Report the malaria status of this cell.
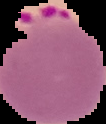
It is parasitized.

Summary:
  - Image size: 106×124 pixels
  - Preparation: thin blood smear
  - Image type: cell region segmented out of the field of view; surrounding area masked to black